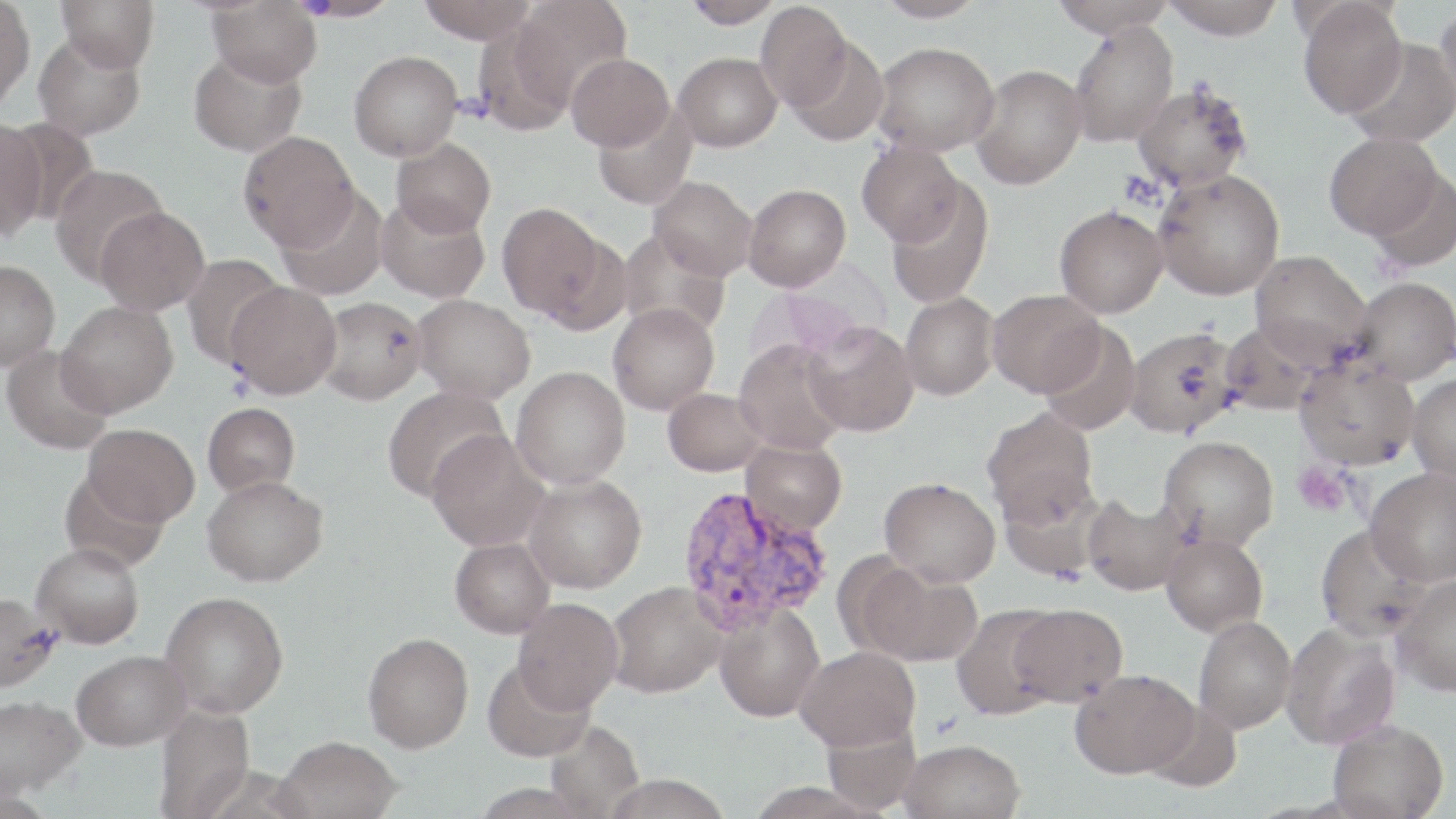

Approximate bounding boxes as (x1, y1, x2, y2) in pixels. Uninfected red blood cell locations: (0, 0, 36, 112), (56, 0, 160, 73), (295, 0, 401, 21), (417, 0, 536, 44), (511, 0, 632, 109), (682, 0, 783, 28), (874, 0, 987, 22), (1051, 0, 1175, 37), (1160, 0, 1286, 40), (1298, 0, 1408, 119), (206, 1, 322, 87), (754, 1, 852, 111), (1436, 3, 1456, 114), (1069, 22, 1179, 146), (33, 32, 146, 140), (786, 37, 890, 146), (1345, 38, 1456, 147), (872, 42, 999, 156), (188, 49, 307, 157), (349, 50, 462, 161), (674, 52, 781, 151), (566, 53, 674, 151), (970, 64, 1087, 190), (1132, 83, 1253, 191), (592, 103, 697, 209), (0, 118, 47, 239), (2, 118, 96, 227), (238, 130, 359, 251), (1324, 132, 1444, 241), (392, 138, 496, 238), (857, 141, 965, 248), (49, 163, 168, 284), (1365, 168, 1456, 272), (1153, 169, 1285, 300), (649, 176, 757, 280), (884, 181, 994, 308), (743, 183, 851, 292), (277, 186, 389, 301), (376, 195, 490, 303), (497, 201, 606, 319), (1054, 205, 1168, 318), (95, 206, 209, 315), (617, 228, 731, 339), (1249, 249, 1374, 367), (181, 254, 287, 368), (0, 260, 60, 370), (1351, 276, 1456, 385), (225, 282, 342, 399), (987, 289, 1105, 397), (900, 291, 999, 400), (412, 294, 536, 403), (316, 296, 426, 404), (56, 301, 177, 417), (607, 303, 719, 415), (803, 321, 918, 436), (1219, 321, 1322, 416), (1039, 322, 1142, 436), (1124, 326, 1242, 437), (734, 339, 850, 455), (2, 345, 114, 455), (1294, 357, 1421, 470), (511, 366, 631, 488), (1407, 373, 1456, 483), (382, 385, 510, 502), (663, 387, 767, 476), (202, 402, 301, 497), (982, 407, 1097, 525), (83, 424, 200, 526), (427, 430, 550, 552), (1158, 435, 1279, 551), (740, 438, 847, 537), (1365, 468, 1456, 587), (58, 469, 170, 571), (202, 474, 328, 587), (523, 474, 646, 593), (880, 477, 1001, 588), (997, 477, 1112, 582), (1082, 493, 1190, 596), (1315, 524, 1430, 642), (1161, 533, 1268, 637), (450, 537, 554, 638), (30, 542, 145, 649), (867, 567, 983, 666), (1390, 575, 1456, 696), (606, 581, 725, 698), (0, 590, 60, 692), (160, 591, 289, 718), (513, 597, 623, 714), (714, 602, 825, 723), (951, 603, 1063, 720), (1010, 603, 1127, 706), (1194, 615, 1296, 733), (1281, 623, 1400, 749), (363, 633, 474, 752), (796, 645, 920, 751), (72, 649, 191, 750), (482, 658, 595, 762), (1070, 669, 1199, 778), (0, 694, 87, 798), (1144, 700, 1243, 792), (153, 705, 255, 818), (821, 717, 922, 814), (1328, 718, 1449, 818), (544, 719, 645, 817), (274, 735, 401, 819), (900, 738, 1025, 819), (601, 774, 732, 819). Plasmodium vivax-infected red blood cell locations: (675, 485, 834, 634). Platelet locations: (1293, 462, 1352, 517). Slide-level diagnosis: Plasmodium vivax. Light microscopy. Image is 1456×819 pixels. May-Grünwald-Giemsa-stained preparation. Single field of view. Thin blood film. Captured at 1000x magnification.